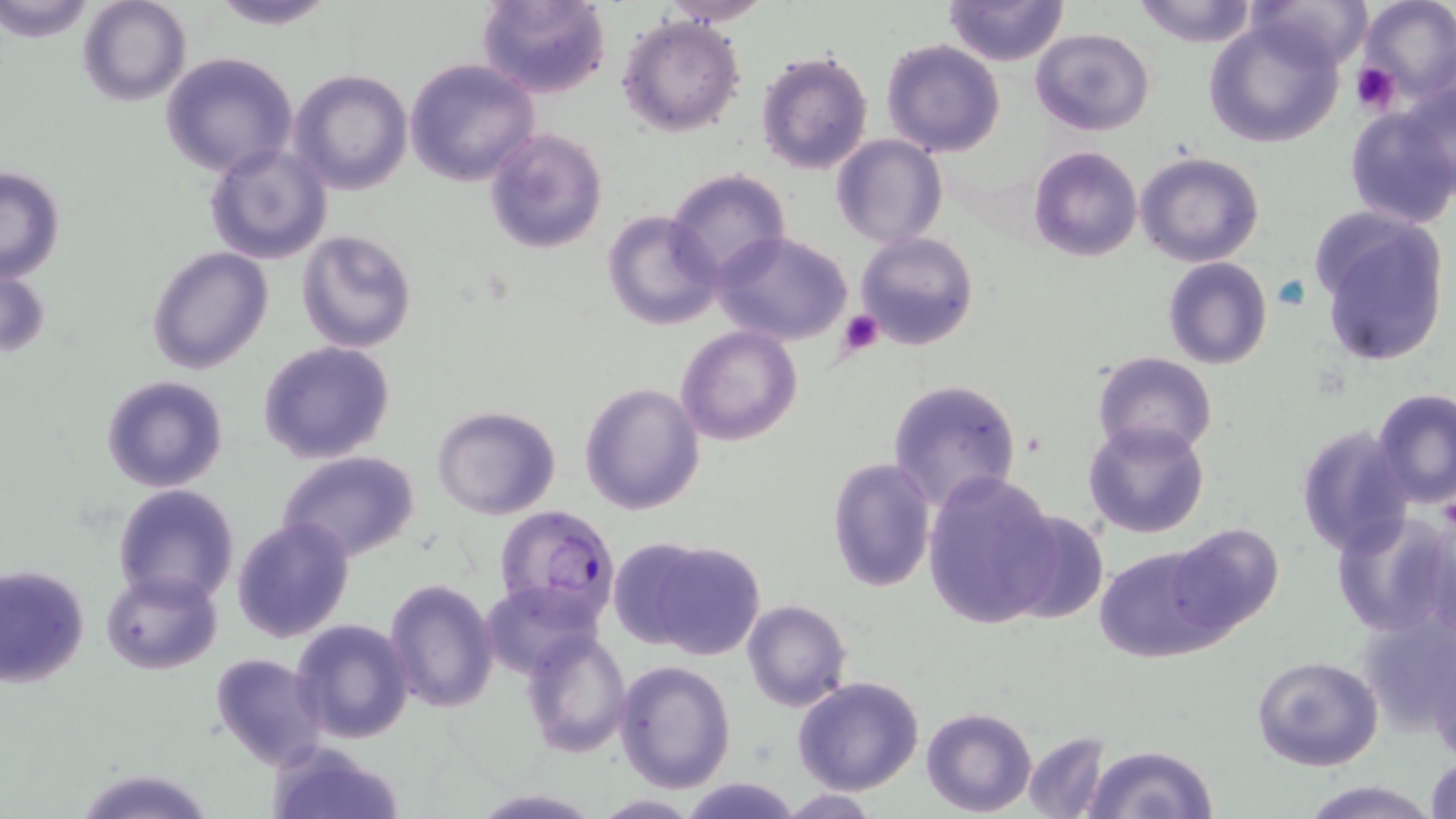
Summary:
  - Coordinate format: approximate bounding boxes as (x1, y1, x2, y2) in pixels
  - Uninfected red blood cell locations: (2, 0, 96, 41), (78, 0, 192, 106), (206, 0, 340, 29), (476, 0, 612, 100), (656, 0, 774, 25), (941, 0, 1070, 66), (1131, 0, 1262, 47), (1245, 0, 1372, 73), (1355, 0, 1456, 108), (1203, 14, 1347, 147), (617, 15, 745, 138), (1032, 28, 1156, 135), (879, 38, 1005, 156), (754, 49, 873, 175), (159, 51, 299, 179), (405, 59, 539, 187), (288, 69, 414, 196), (1404, 76, 1456, 192), (1343, 104, 1456, 229), (484, 128, 608, 254), (831, 134, 947, 248), (205, 142, 331, 264), (1028, 145, 1141, 261), (1135, 151, 1265, 267), (0, 166, 66, 282), (665, 167, 792, 283), (602, 209, 722, 332), (1313, 214, 1451, 368), (296, 231, 417, 353), (713, 232, 852, 346), (856, 232, 978, 348), (146, 247, 273, 373), (1161, 256, 1272, 370), (1, 261, 50, 362), (676, 324, 802, 445), (257, 341, 398, 465), (1092, 351, 1218, 458), (101, 375, 228, 493), (886, 377, 1024, 513), (577, 381, 706, 516), (1373, 390, 1456, 509), (431, 404, 562, 519), (1083, 420, 1209, 539), (1294, 424, 1414, 559), (277, 452, 419, 563), (826, 457, 937, 592), (921, 470, 1063, 631), (112, 484, 240, 608), (1000, 507, 1110, 626), (1331, 507, 1454, 637), (231, 516, 355, 644), (1166, 524, 1282, 639), (632, 537, 767, 661), (1094, 539, 1228, 662), (0, 563, 90, 687), (102, 570, 221, 675), (384, 578, 499, 714), (481, 581, 596, 679), (741, 600, 851, 712), (1356, 603, 1456, 737), (289, 617, 416, 743), (756, 628, 884, 773), (520, 629, 632, 756), (1429, 642, 1456, 769), (210, 653, 329, 771), (1251, 655, 1384, 772), (615, 659, 737, 794), (792, 675, 924, 795), (920, 706, 1036, 816), (1022, 731, 1111, 817), (265, 740, 406, 819), (1081, 744, 1219, 819), (1424, 752, 1456, 819), (73, 766, 217, 819), (678, 778, 805, 818), (1296, 781, 1441, 819)
  - Platelet locations: (1350, 62, 1402, 114), (838, 309, 883, 357)
  - Plasmodium falciparum-infected red blood cell locations: (493, 504, 619, 624)
  - Slide-level diagnosis: Plasmodium falciparum
  - Stain: May-Grünwald-Giemsa
  - Preparation: thin blood film
  - Modality: optical microscopy
  - Image size: 1456×819 pixels
  - Field of view: single
  - Magnification: 1000x